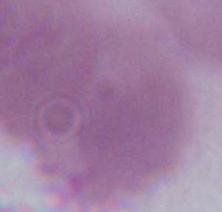
Summary:
  - Magnification: 1000x
  - Identification: red blood cell
  - Modality: photomicrograph